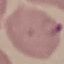

Summary:
  - Malaria status: parasitized
  - Capture: smartphone camera at the microscope eyepiece
  - Preparation: thin blood film
  - Image type: cell patch, automatically extracted from a larger field of view and resized to 64 × 64 pixels
  - Stain: Giemsa